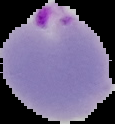
{
  "preparation": "thin blood film",
  "image_type": "cell region segmented out of the field of view; surrounding area masked to black",
  "malaria_status": "parasitized",
  "image_size": "115×124 pixels"
}